Classify this cell by malaria status.
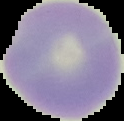
It is uninfected.

Cell region segmented out of the field of view; the surrounding area is masked to black. Image is 124×121 pixels. From a thin blood film.